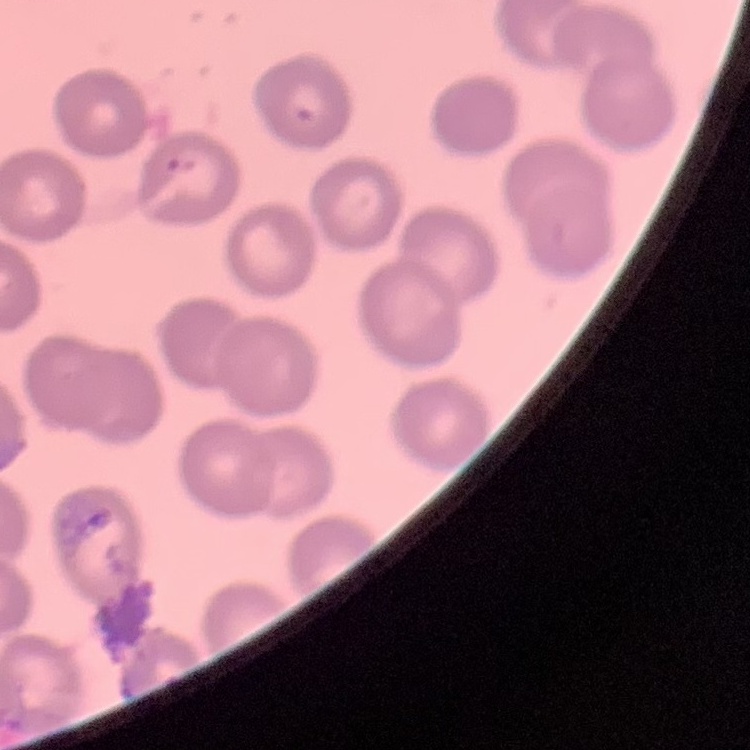 The red blood cells exhibit no rouleaux formation. Stained with either Field's or Giemsa. Thin blood film. Square crop of a larger photomicrograph.